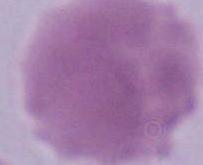

identification = erythrocyte
modality = photomicrograph
magnification = 1000x